State which parasite is depicted.
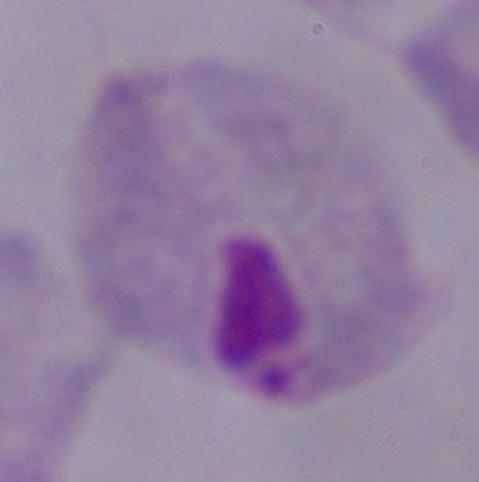

This is a trichomonad.

{
  "magnification": "1000x",
  "modality": "photomicrograph"
}